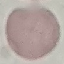 Malaria status: uninfected. Photographed with a smartphone camera at the microscope eyepiece. Giemsa-stained preparation. Thin smear of blood. Cell patch, automatically extracted from a larger field of view and resized to 64 × 64 pixels.